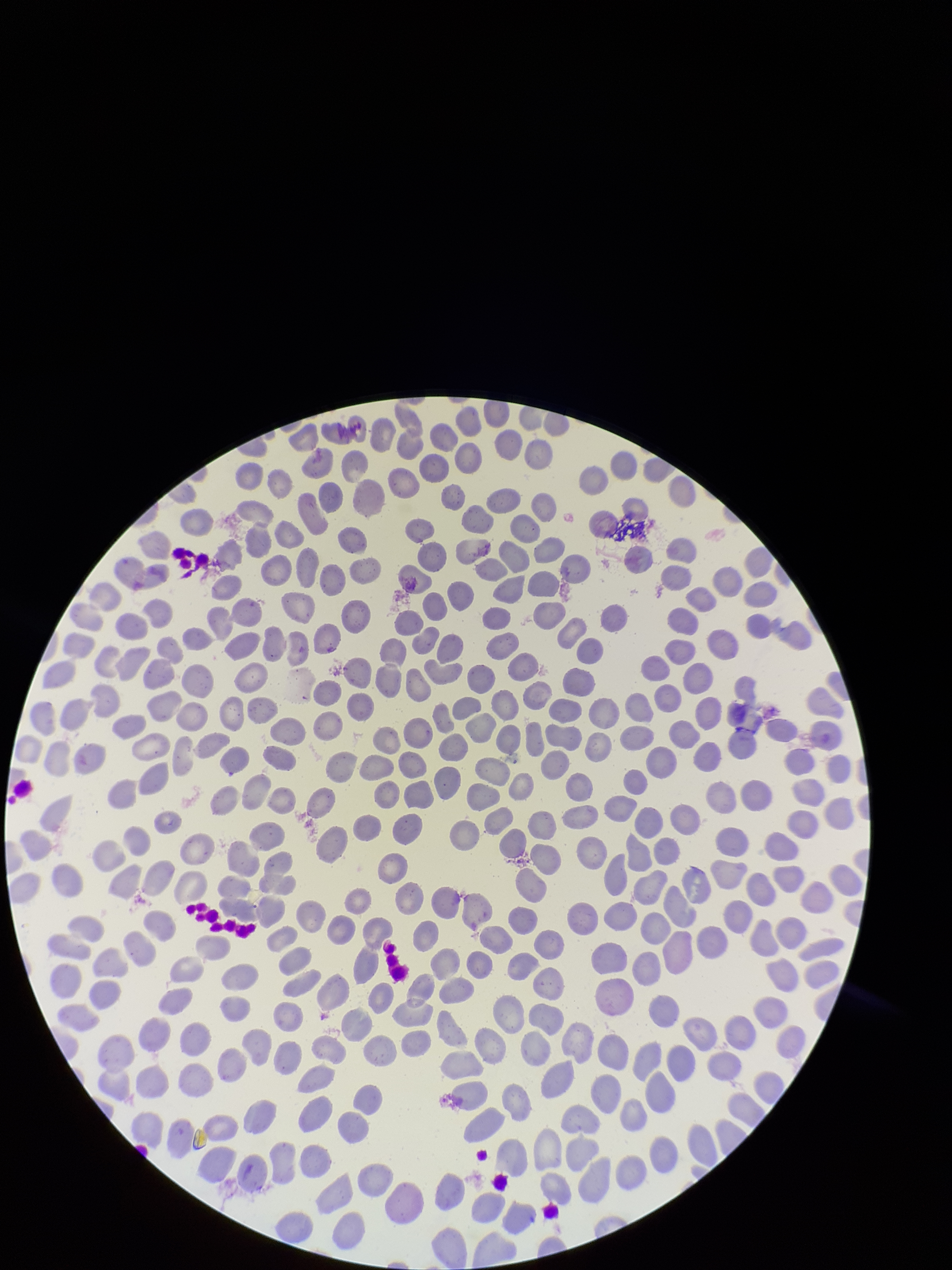

{
  "capture": "smartphone photograph through the microscope eyepiece",
  "image_size": "952×1270 pixels",
  "red_blood_cell_count": 248,
  "parasitized_red_blood_cells": "none identified",
  "preparation": "thin blood smear",
  "parasitized_red_blood_cell_count": 0,
  "patient_malaria_status": "negative",
  "stain": "Giemsa",
  "field_of_view": "single"
}